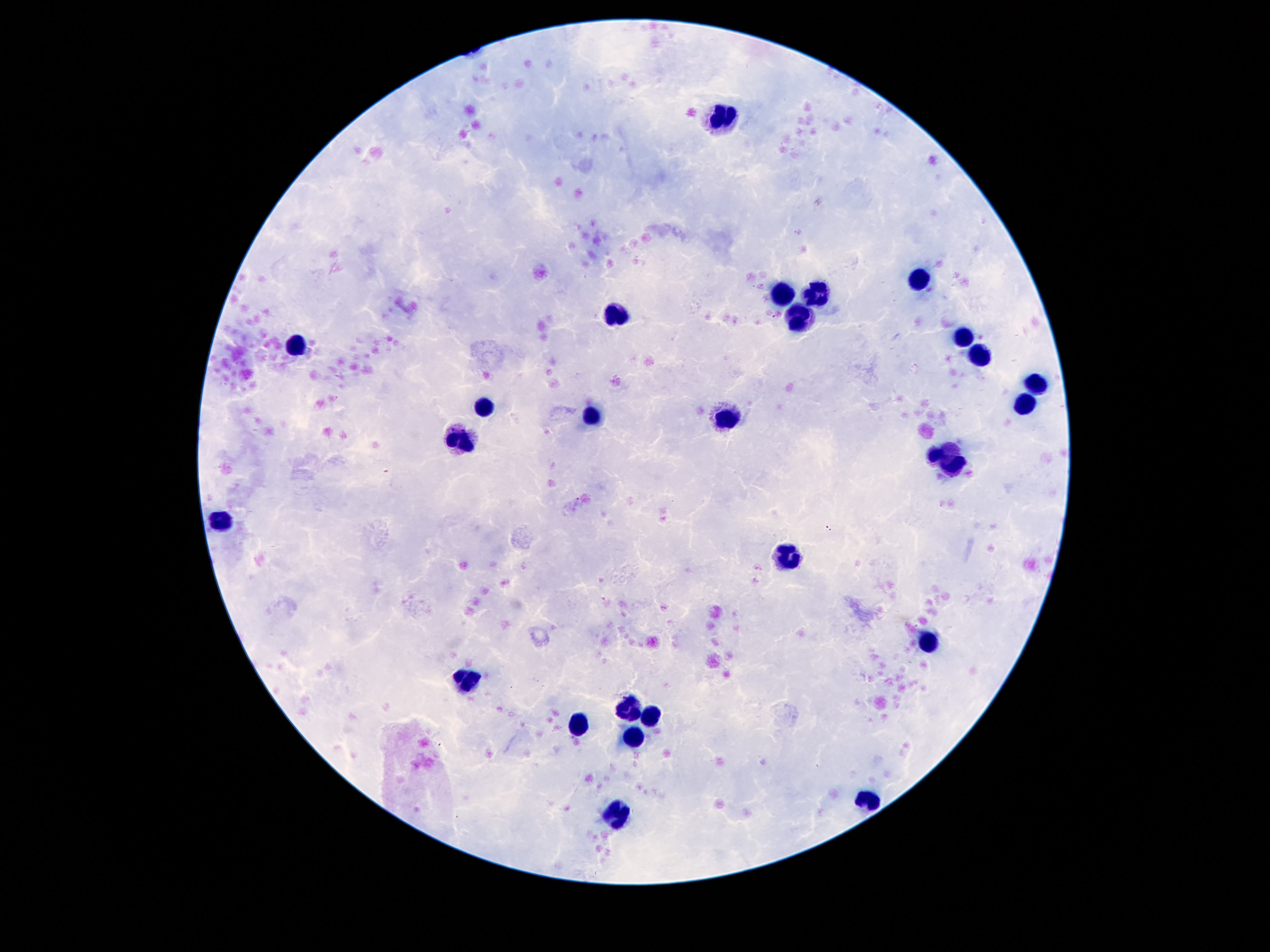
Approximate centers as {x, y} in pixels. Leukocyte locations: {725, 116}, {918, 280}, {782, 296}, {819, 296}, {617, 314}, {801, 316}, {961, 340}, {295, 346}, {979, 354}, {1036, 383}, {1024, 404}, {483, 409}, {592, 417}, {727, 419}, {461, 439}, {948, 458}, {221, 519}, {787, 555}, {926, 643}, {465, 680}, {625, 707}, {655, 715}, {578, 727}, {631, 737}, {868, 797}, {614, 816}. Patient malaria status: not infected. 100x magnification. Giemsa-stained preparation. Single field of view. Image is 1270×952 pixels. Thick blood smear. Photographed through the microscope eyepiece with a smartphone camera.